Report the malaria status of this cell.
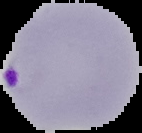
Parasitized.

image_size: 142×133 pixels
image_type: segmented cell region with the area outside set to black
preparation: thin blood film